Identify the parasite.
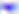

Toxoplasma gondii.

modality = photomicrograph
magnification = 400x